Assess the morphology of the red blood cells.
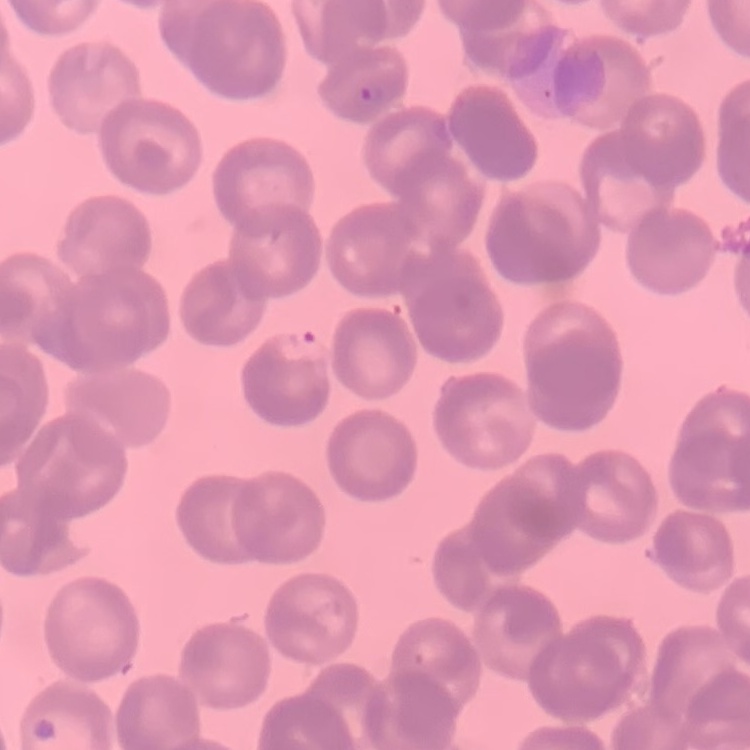
They show rouleaux formation.

Summary:
  - Image type: one tile cut from a larger photomicrograph
  - Preparation: thin peripheral smear
  - Stain: Field's or Giemsa